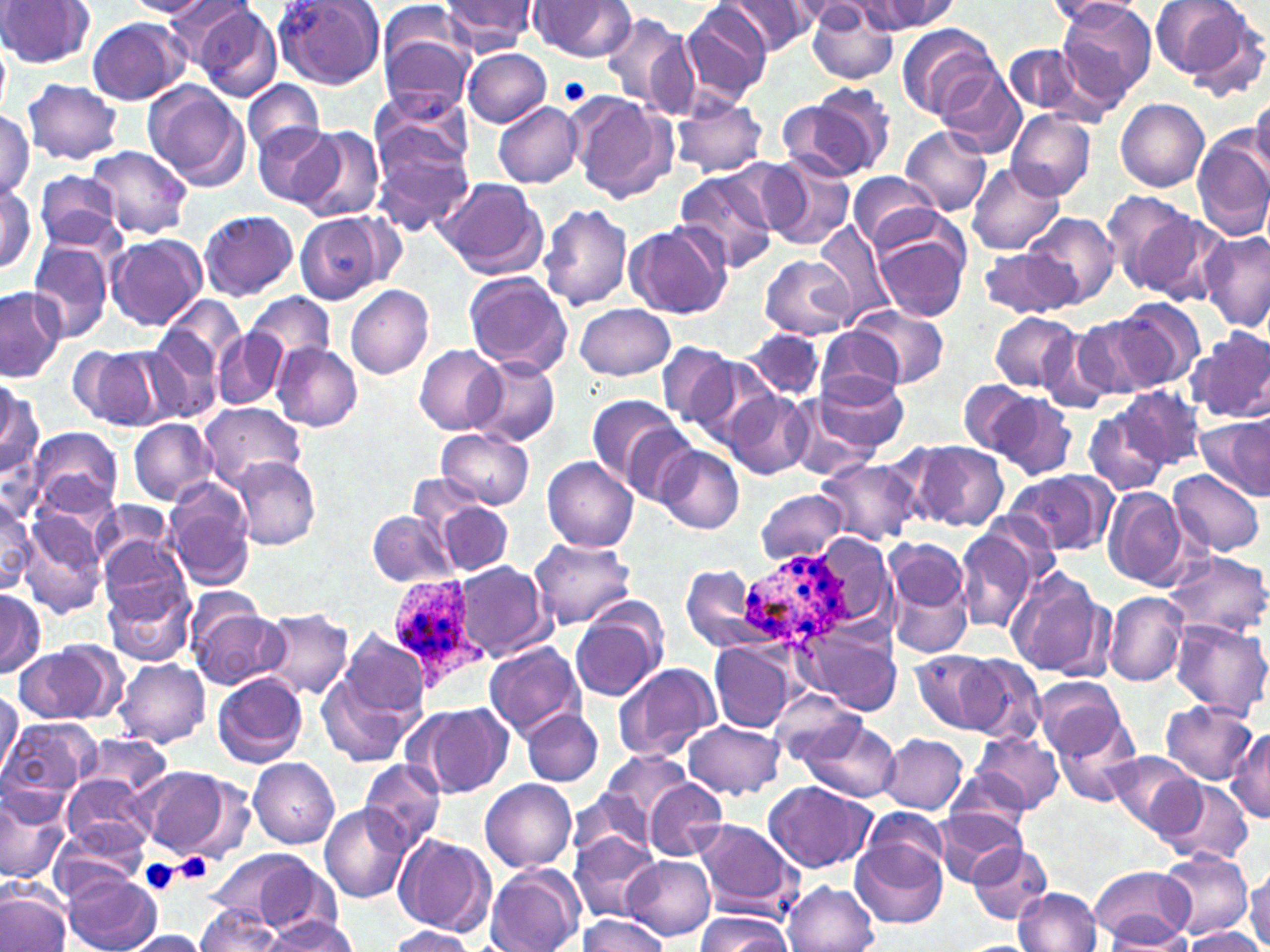
slide-level diagnosis = Plasmodium ovale
preparation = thin blood smear
platelet locations = approximate bounding boxes as [x1, y1, x2, y2] in pixels: [559, 76, 591, 108], [172, 852, 214, 884], [139, 859, 181, 895]
stain = May-Grünwald-Giemsa
modality = light microscopy
Plasmodium ovale-infected red blood cell locations = approximate bounding boxes as [x1, y1, x2, y2] in pixels: [739, 549, 858, 651], [384, 580, 485, 689]
field of view = single
image size = 1270×952 pixels
uninfected red blood cell locations = approximate bounding boxes as [x1, y1, x2, y2] in pixels: [0, 0, 94, 68], [126, 0, 213, 16], [163, 0, 261, 76], [854, 0, 955, 36], [1149, 0, 1260, 84], [272, 1, 384, 89], [526, 1, 637, 62], [1057, 1, 1155, 106], [437, 2, 535, 53], [679, 2, 773, 105], [723, 2, 821, 54], [1050, 2, 1147, 25], [807, 5, 899, 84], [189, 6, 281, 102], [599, 11, 695, 114], [87, 17, 191, 105], [895, 23, 1000, 119], [378, 24, 476, 116], [0, 39, 11, 120], [1005, 43, 1088, 118], [462, 48, 551, 126], [938, 63, 1023, 156], [22, 79, 124, 165], [244, 79, 324, 159], [141, 82, 251, 192], [786, 84, 895, 184], [370, 92, 473, 180], [569, 92, 676, 204], [1250, 94, 1270, 177], [670, 95, 768, 179], [1116, 99, 1209, 192], [494, 102, 582, 187], [0, 110, 35, 199], [1007, 110, 1096, 200], [254, 123, 338, 206], [294, 126, 385, 222], [900, 127, 992, 215], [1192, 133, 1270, 242], [372, 134, 472, 234], [88, 145, 193, 238], [757, 155, 857, 251], [967, 161, 1064, 255], [673, 167, 778, 270], [33, 170, 124, 253], [847, 170, 941, 253], [436, 176, 548, 279], [0, 180, 40, 275], [1102, 189, 1199, 291], [539, 204, 632, 311], [198, 209, 299, 300], [1135, 210, 1233, 308], [1027, 212, 1119, 308], [295, 213, 385, 306], [814, 220, 896, 325], [624, 223, 729, 320], [1200, 232, 1270, 332], [105, 234, 206, 330], [874, 235, 969, 321], [27, 239, 115, 342], [977, 248, 1073, 318], [758, 255, 855, 338], [463, 271, 573, 376], [345, 283, 433, 379], [0, 286, 66, 380], [247, 292, 335, 370], [158, 294, 246, 379], [1113, 298, 1205, 389], [575, 303, 676, 380], [847, 304, 950, 389], [990, 312, 1082, 393], [1070, 313, 1167, 402], [1039, 327, 1116, 412], [817, 328, 905, 403], [1187, 328, 1270, 423], [142, 329, 224, 424], [215, 329, 289, 410], [745, 329, 826, 401], [658, 341, 741, 427], [271, 342, 363, 431], [68, 345, 169, 430], [414, 345, 508, 434], [470, 356, 560, 446], [682, 356, 779, 450], [813, 373, 909, 455], [958, 379, 1032, 455], [0, 381, 42, 484], [1120, 385, 1208, 469], [988, 390, 1078, 480], [724, 391, 812, 480], [585, 392, 686, 490], [788, 396, 879, 480], [197, 402, 308, 492], [1083, 406, 1170, 496], [1197, 415, 1270, 498], [128, 419, 217, 504], [28, 426, 122, 518], [619, 427, 702, 510], [437, 428, 534, 509], [902, 440, 1009, 532], [657, 446, 744, 534], [229, 456, 321, 550], [542, 457, 640, 551], [816, 457, 921, 544], [1166, 469, 1264, 558], [1005, 470, 1114, 557], [164, 478, 256, 588], [421, 486, 514, 577], [1102, 487, 1192, 591], [755, 489, 849, 566], [0, 496, 35, 596], [92, 501, 173, 575], [367, 510, 459, 587], [21, 511, 109, 618], [953, 520, 1046, 634], [528, 536, 637, 628], [885, 536, 970, 619], [99, 539, 192, 633], [1163, 550, 1270, 638], [453, 561, 553, 661], [886, 561, 975, 659], [682, 566, 761, 652], [1005, 566, 1112, 679], [102, 580, 193, 668], [0, 589, 44, 676], [1104, 591, 1189, 686], [186, 599, 286, 691], [259, 608, 355, 699], [570, 612, 665, 701], [1167, 619, 1270, 715], [797, 621, 902, 717], [337, 628, 432, 723], [710, 641, 798, 733], [484, 642, 583, 738], [14, 645, 117, 725], [912, 650, 1002, 733], [958, 655, 1046, 742], [114, 658, 211, 749], [611, 662, 722, 761], [316, 670, 418, 768], [212, 672, 309, 768], [1034, 676, 1128, 759], [0, 689, 20, 778], [770, 689, 867, 771], [1160, 699, 1259, 785], [417, 702, 511, 798], [521, 709, 604, 787], [1052, 715, 1143, 807], [2, 718, 100, 807], [801, 719, 899, 802], [684, 720, 785, 801], [1226, 728, 1270, 822], [972, 731, 1064, 813], [75, 733, 173, 803], [880, 733, 969, 815], [599, 750, 693, 829], [1106, 751, 1204, 836], [247, 757, 339, 846], [358, 760, 445, 851], [142, 767, 241, 861], [944, 769, 1031, 844], [62, 774, 153, 852], [481, 779, 577, 873], [645, 780, 728, 861], [763, 780, 873, 874], [1157, 782, 1253, 865], [0, 789, 68, 882], [567, 790, 653, 861], [319, 805, 413, 904], [932, 807, 1024, 886], [861, 809, 951, 884], [691, 819, 799, 916], [50, 824, 150, 897], [570, 831, 661, 922], [393, 832, 495, 936], [851, 841, 946, 928], [968, 842, 1051, 925], [203, 848, 325, 933], [1157, 849, 1251, 940], [624, 856, 715, 940], [485, 864, 584, 952], [1090, 865, 1195, 944], [1246, 869, 1270, 948], [65, 873, 161, 952], [250, 879, 351, 952], [782, 880, 879, 952], [1013, 888, 1102, 952], [0, 891, 70, 952], [194, 904, 285, 952], [694, 913, 789, 952], [576, 914, 670, 952], [261, 915, 358, 949], [1102, 920, 1193, 948], [385, 925, 477, 952], [1184, 928, 1265, 951], [124, 931, 207, 952]
magnification = 1000x